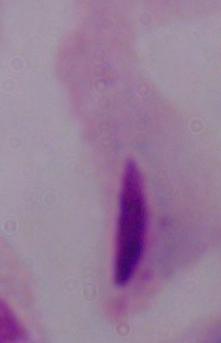

Summary:
  - Identification: trichomonad
  - Modality: micrograph
  - Magnification: 1000x